Comment on the morphology of the erythrocytes.
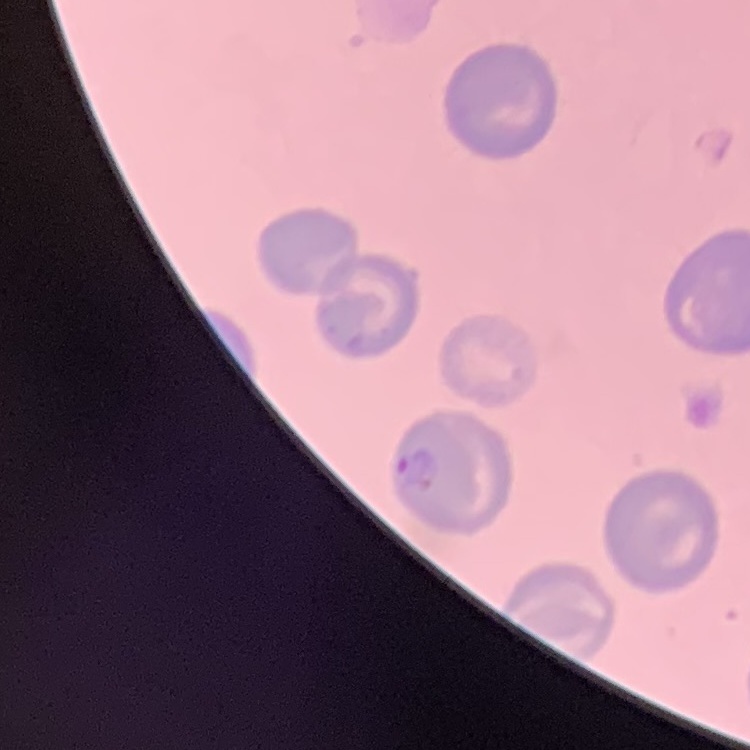
No rouleaux formation.

{
  "image_type": "one tile cut from a larger photomicrograph",
  "preparation": "thin blood smear",
  "stain": "Field's or Giemsa"
}